State which parasite is depicted.
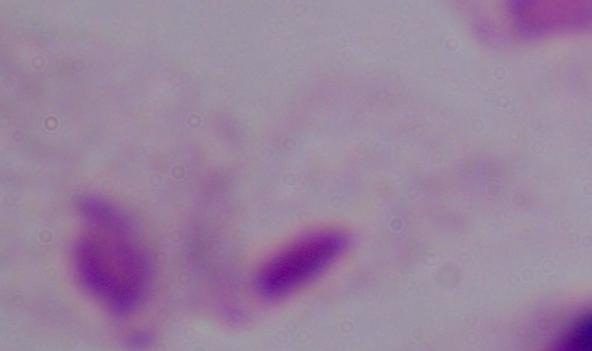
A trichomonad.

Summary:
  - Magnification: 1000x
  - Modality: micrograph